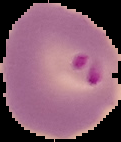

{
  "image_type": "cell region segmented out of the field of view; surrounding area masked to black",
  "image_size": "121×142 pixels",
  "preparation": "thin blood smear",
  "result": "malaria parasites identified"
}